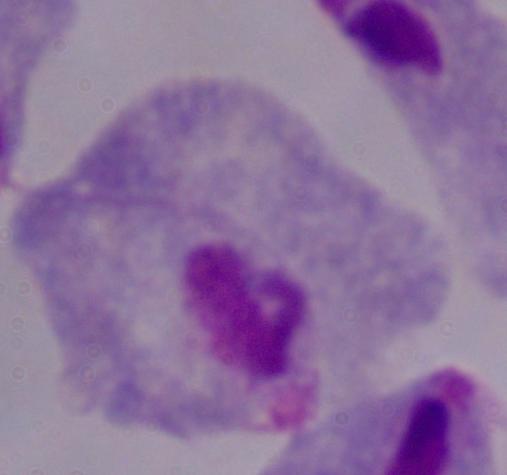

identification = trichomonad
magnification = 1000x
modality = micrograph